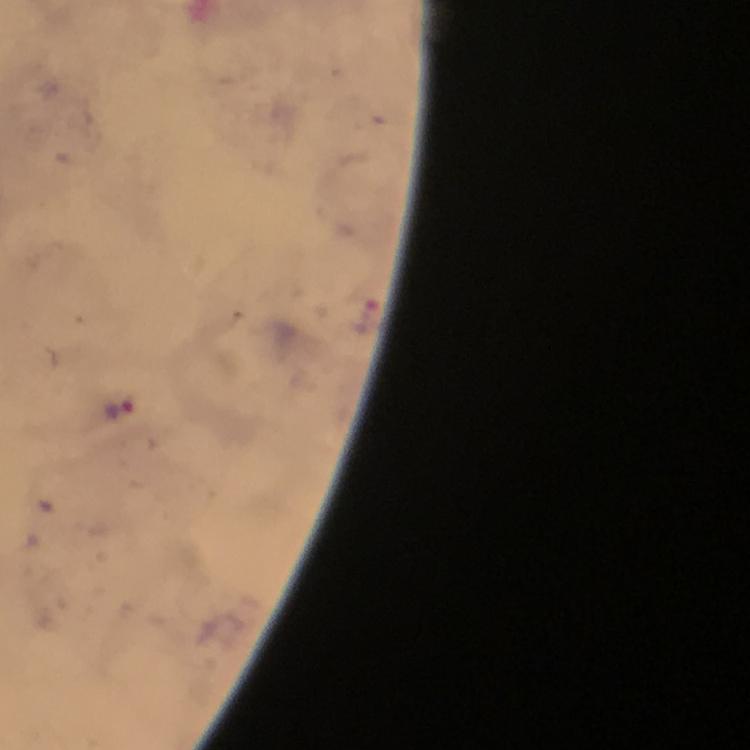

Approximate centers as [x, y] in pixels.
Summary:
  - Malaria parasite locations: [117, 412]
  - Preparation: thick blood smear
  - Immersion oil: applied
  - Capture: smartphone camera through the microscope
  - Cropped from: one field of view
  - Context: from a diagnostic examination for malaria
  - Image size: 750×750 pixels
  - Stain: Giemsa
  - Magnification: 100x